Classify this cell by malaria status.
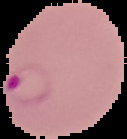
Parasitized.

Summary:
  - Image type: segmented cell region with the area outside set to black
  - Image size: 127×139 pixels
  - Preparation: thin blood smear